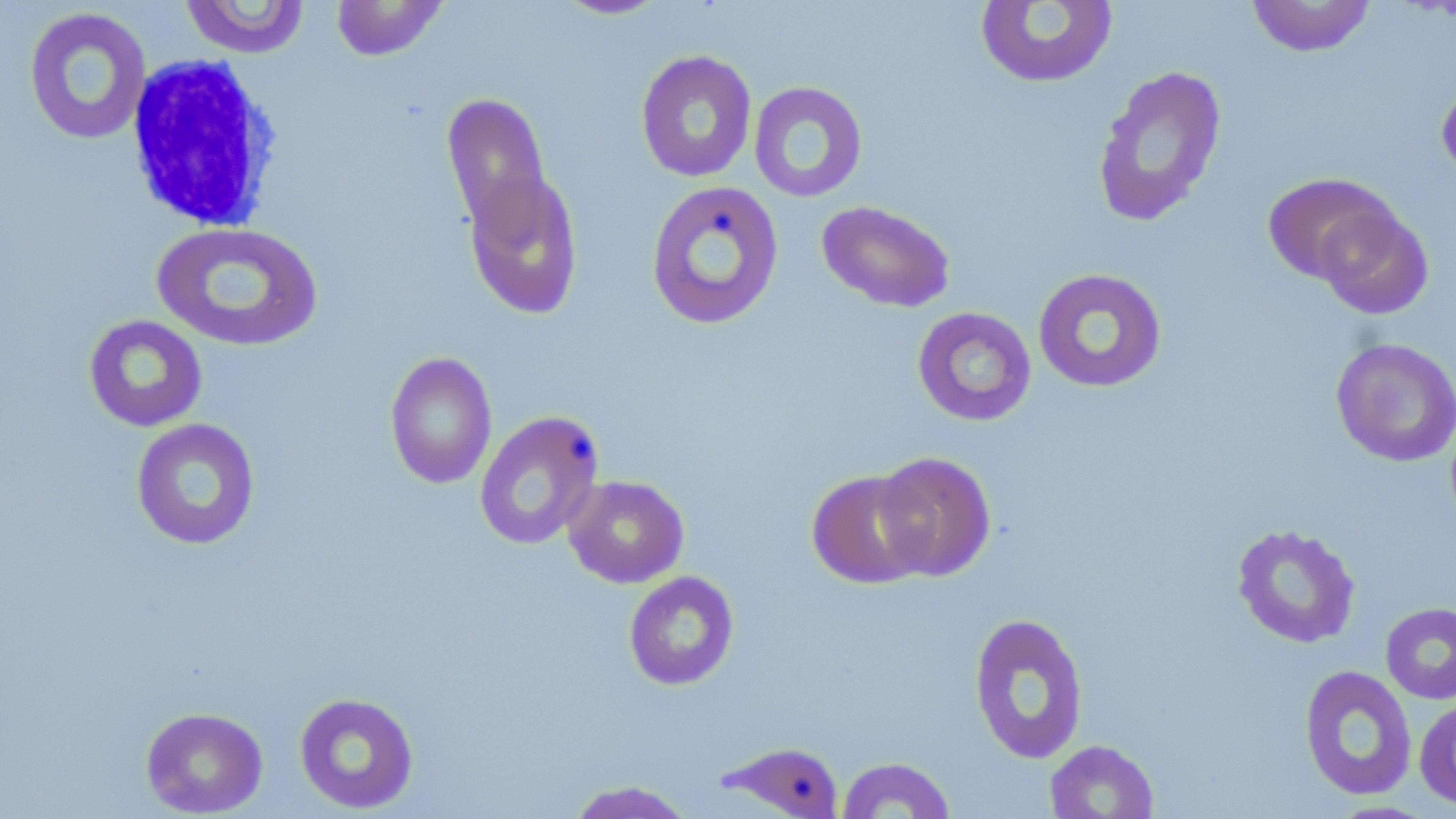

Approximate bounding boxes as (x1, y1, x2, y2) in pixels. White blood cell locations: (122, 54, 287, 235). Uninfected red blood cell locations: (179, 0, 312, 58), (331, 0, 449, 61), (551, 0, 672, 20), (1246, 0, 1376, 57), (975, 1, 1119, 89), (22, 7, 152, 146), (635, 50, 758, 183), (1091, 65, 1228, 228), (1435, 75, 1456, 183), (748, 81, 868, 202), (441, 92, 553, 234), (462, 165, 585, 320), (1262, 172, 1399, 284), (645, 179, 785, 331), (816, 201, 956, 313), (1313, 202, 1434, 320), (151, 221, 324, 353), (1032, 268, 1167, 393), (912, 307, 1037, 426), (83, 315, 208, 432), (1330, 337, 1456, 468), (384, 352, 498, 488), (474, 411, 604, 551), (131, 418, 261, 551), (872, 451, 997, 582), (806, 469, 931, 589), (563, 475, 689, 588), (1231, 523, 1361, 649), (623, 570, 740, 691), (1380, 602, 1456, 704), (968, 612, 1090, 764), (1299, 664, 1417, 801), (293, 692, 420, 814), (1414, 697, 1456, 811), (140, 707, 268, 817), (715, 740, 846, 818), (1044, 740, 1159, 819), (835, 756, 957, 818), (565, 779, 697, 818). Slide-level diagnosis: negative for blood parasites. Image is 1456×819 pixels. Light microscopy. Single field of view. May-Grünwald-Giemsa-stained preparation. Thin blood film. 1000x magnification.